Locate every blood parasite and identify its species.
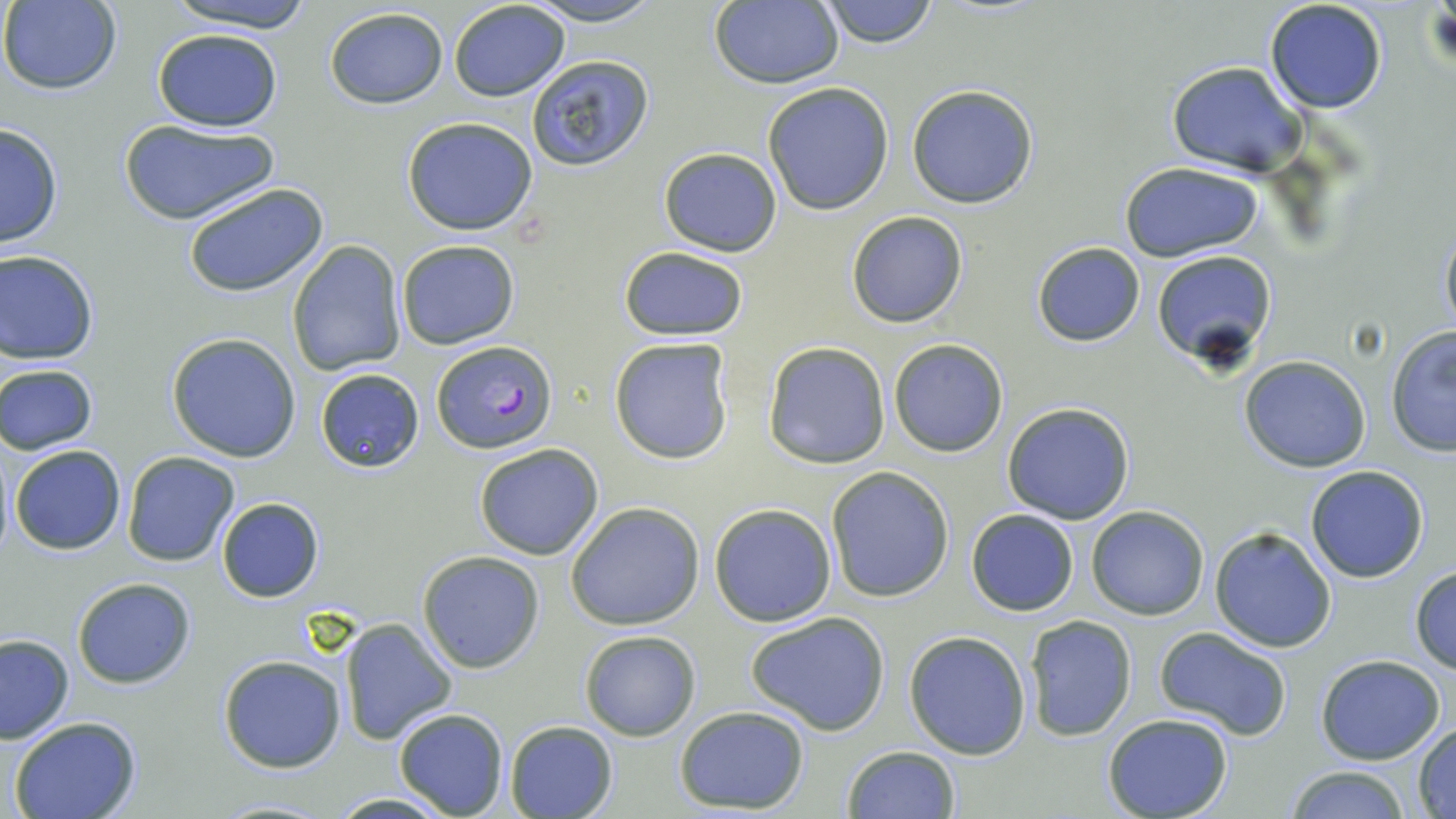
Approximate bounding boxes as [x1, y1, x2, y2] in pixels.
Plasmodium falciparum-infected red blood cells: [431, 340, 555, 452].
No Plasmodium ovale, Plasmodium malariae, Plasmodium vivax, Babesia divergens, or Trypanosoma brucei observed.

slide_level_diagnosis: Plasmodium falciparum
image_size: 1456×819 pixels
stain: May-Grünwald-Giemsa
modality: optical microscopy
field_of_view: single
magnification: 1000x
uninfected_red_blood_cell_locations: 'approximate bounding boxes as [x1, y1, x2, y2] in pixels: [162, 0, 319, 31], [448, 0, 570, 102], [521, 0, 665, 26], [818, 0, 941, 50], [0, 1, 123, 94], [710, 1, 842, 90], [1263, 1, 1388, 115], [323, 7, 448, 110], [152, 27, 283, 133], [524, 55, 656, 172], [1166, 61, 1307, 178], [761, 82, 896, 215], [906, 84, 1039, 209], [402, 116, 540, 237], [119, 118, 279, 226], [0, 122, 64, 248], [658, 146, 782, 257], [1119, 161, 1264, 263], [182, 180, 332, 299], [846, 210, 970, 329], [1439, 217, 1456, 342], [396, 239, 521, 350], [287, 240, 408, 376], [1031, 242, 1144, 347], [618, 247, 749, 342], [0, 249, 100, 364], [1149, 249, 1277, 368], [1385, 327, 1455, 458], [167, 332, 303, 462], [608, 337, 736, 465], [889, 339, 1009, 457], [761, 342, 890, 469], [1240, 355, 1372, 473], [0, 364, 99, 454], [314, 367, 424, 475], [1002, 401, 1135, 524], [473, 443, 605, 561], [10, 444, 126, 554], [121, 451, 239, 568], [1305, 465, 1430, 583], [826, 467, 954, 603], [216, 497, 323, 602], [565, 501, 704, 631], [708, 502, 837, 627], [1085, 505, 1211, 620], [965, 509, 1080, 617], [1209, 525, 1337, 653], [416, 550, 545, 674], [1409, 563, 1456, 673], [72, 577, 196, 689], [746, 612, 891, 736], [1022, 614, 1137, 741], [337, 618, 458, 747], [1155, 627, 1293, 741], [579, 630, 701, 742], [904, 630, 1032, 759], [0, 634, 74, 744], [218, 655, 346, 773], [1316, 655, 1447, 765], [674, 706, 810, 813], [392, 709, 509, 819], [1101, 713, 1235, 819], [8, 715, 144, 819], [503, 720, 617, 818], [1413, 724, 1456, 815], [841, 743, 961, 819], [1285, 765, 1412, 819], [326, 792, 460, 819], [207, 798, 337, 817]'
preparation: thin blood film